Assess this cell for malaria.
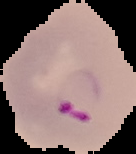

It is parasitized.

The area outside the segmented cell region is set to black. Image is 136×154 pixels. From a thin blood film.